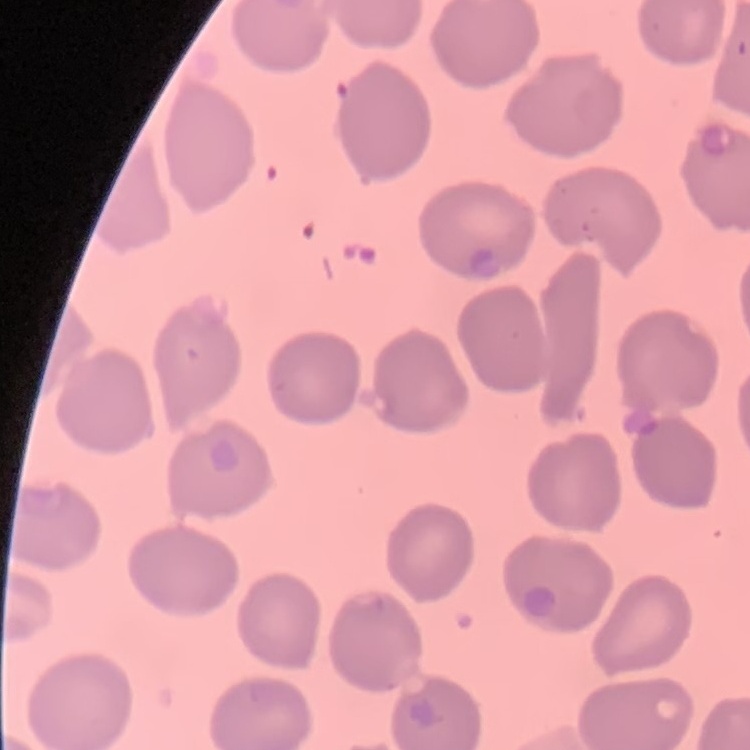

erythrocyte_morphology: no rouleaux formation
preparation: thin blood film
image_type: one tile cut from a larger photomicrograph
stain: Field's or Giemsa